Name the parasite shown.
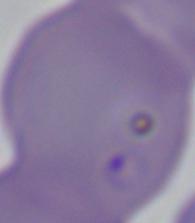
Babesia.

1000x magnification. Micrograph.